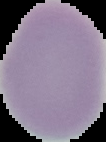
Summary:
  - Image type: segmented cell region on a black background
  - Image size: 106×142 pixels
  - Malaria status: uninfected
  - Preparation: thin blood film